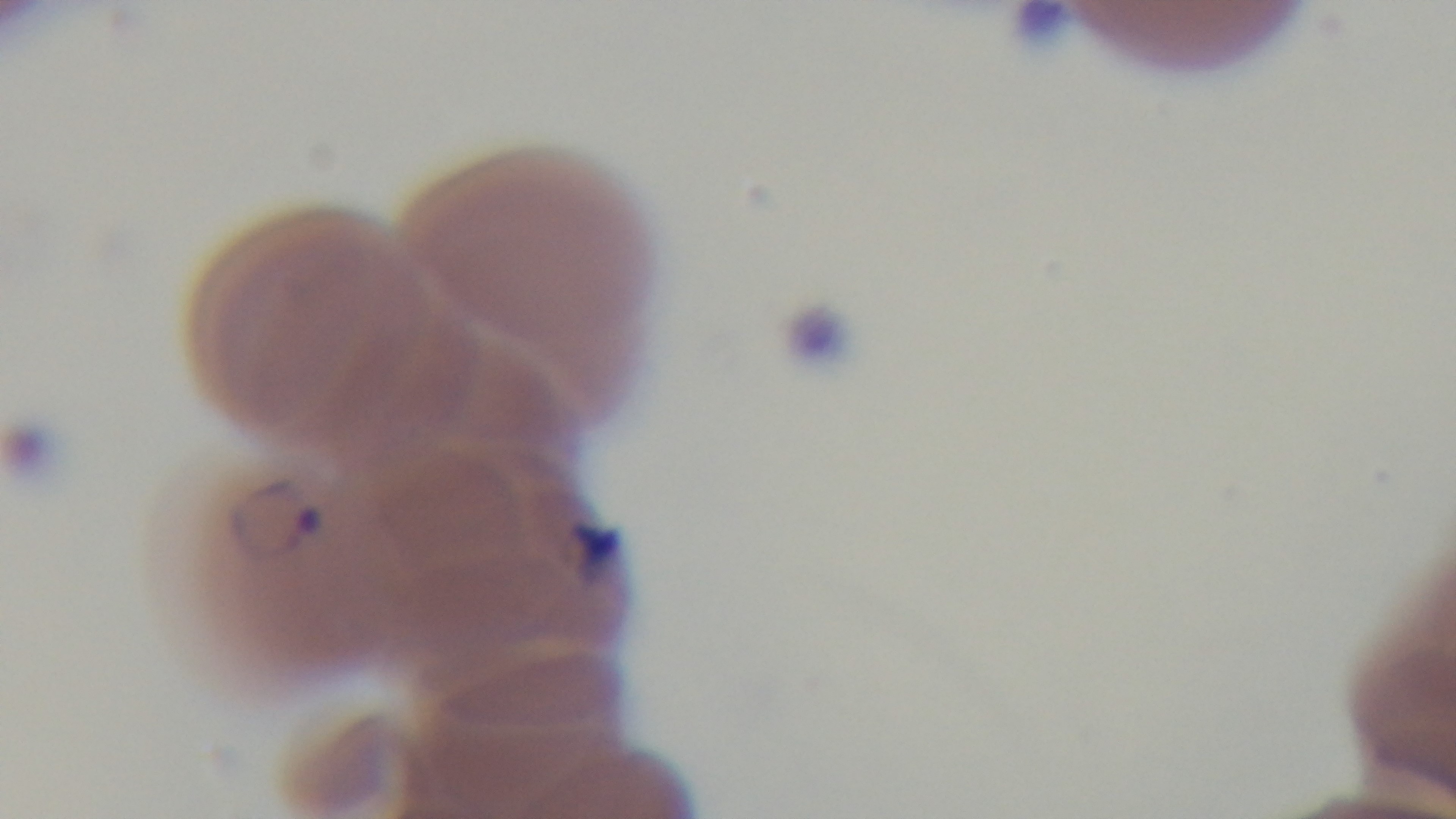 One field from the slide. Captured with a mounted 4K digital camera. Malaria status: infected. 100x oil-immersion objective. Photomicrograph. Giemsa-stained. Preparation: thin smear.